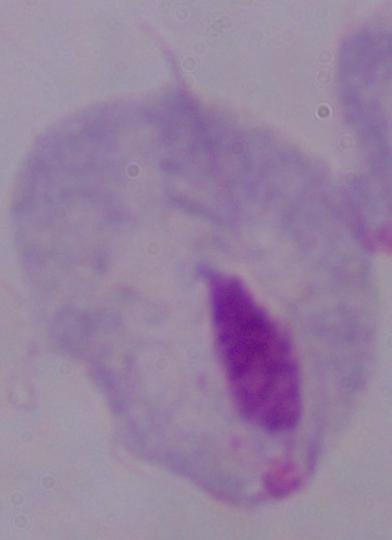
modality = photomicrograph
magnification = 1000x
identification = trichomonad